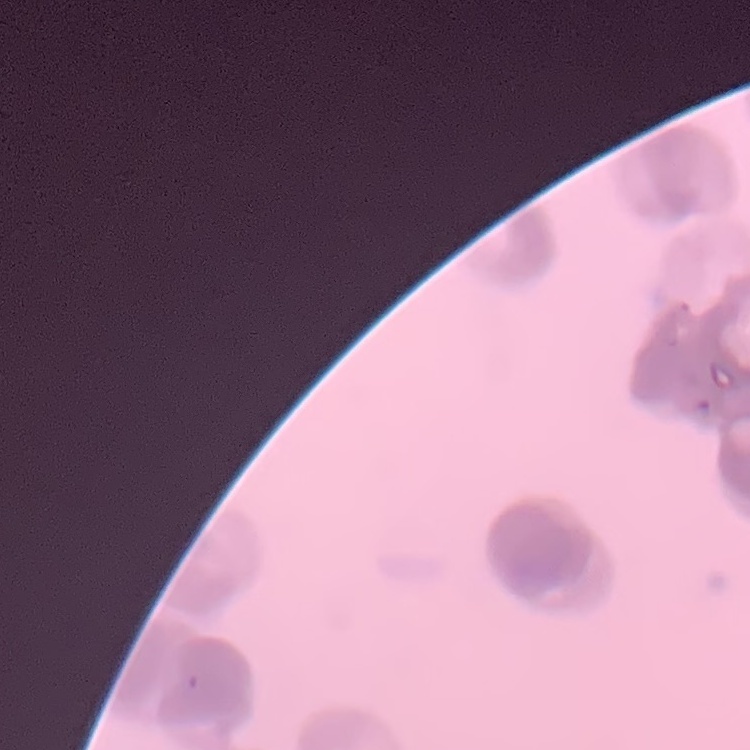
red blood cell morphology = rouleaux formation
preparation = thin blood smear
image type = one tile cut from a larger photomicrograph
stain = Field's or Giemsa